Identify the parasite.
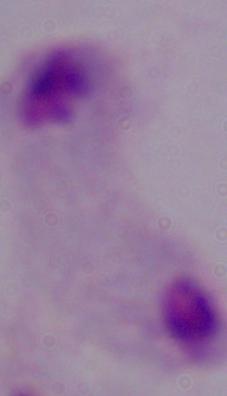
This is a trichomonad.

modality: photomicrograph
magnification: 1000x